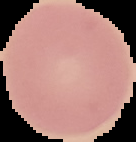
preparation = thin blood smear
image size = 136×142 pixels
malaria status = uninfected
image type = segmented cell region on a black background